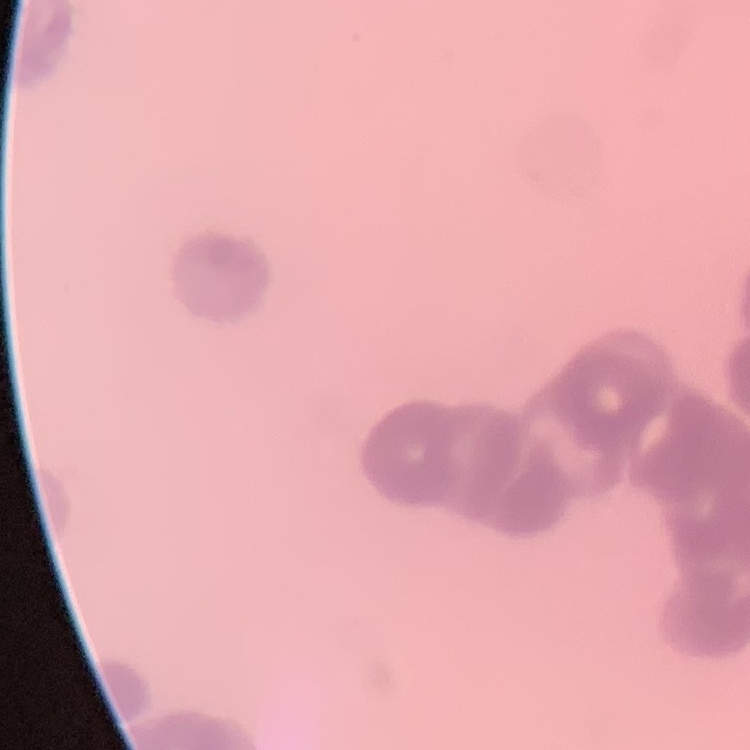
Summary:
  - Red blood cell morphology: rouleaux formation
  - Preparation: thin peripheral smear
  - Stain: Field's or Giemsa
  - Image type: one tile cut from a larger photomicrograph